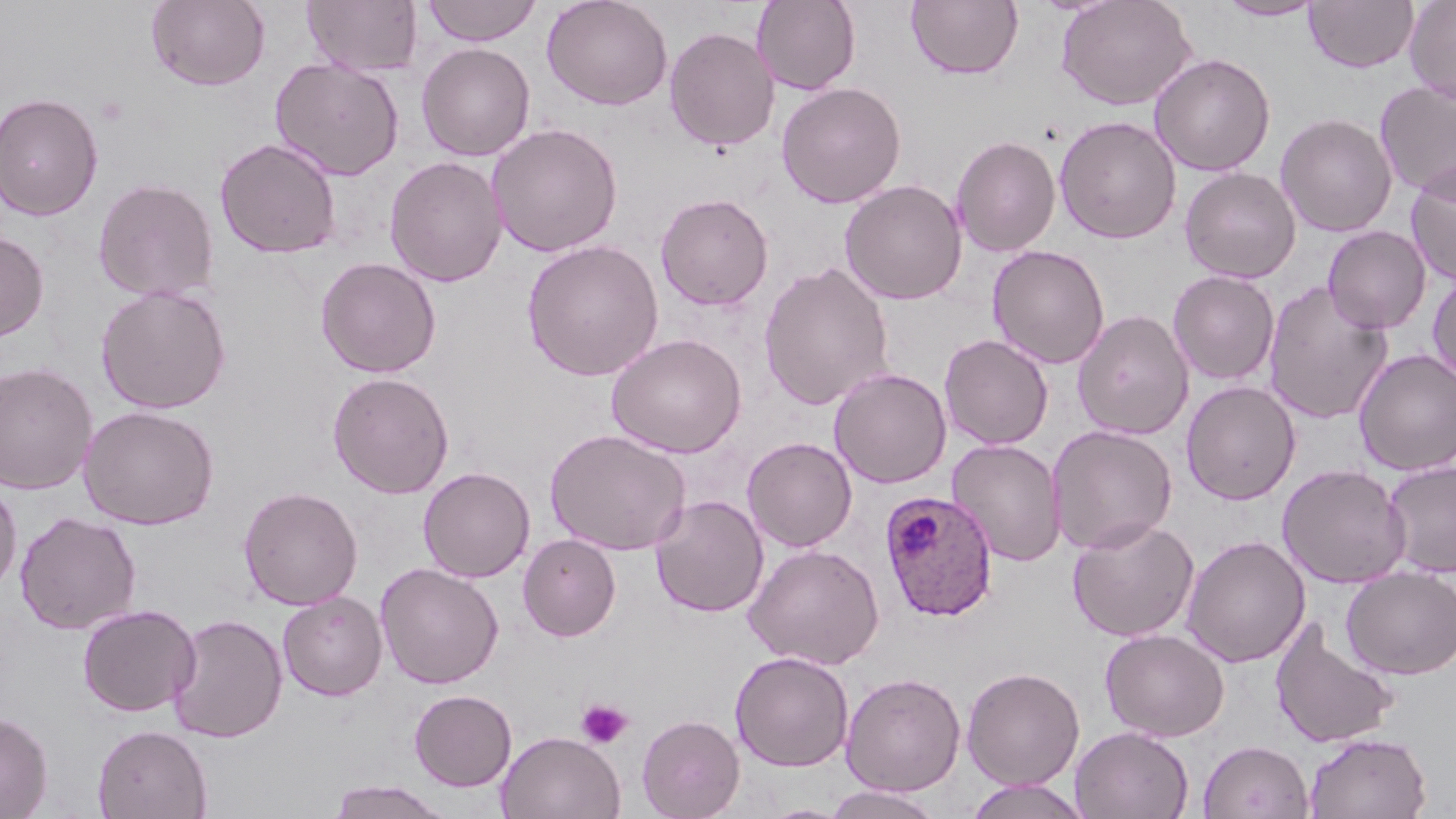
Summary:
  - Coordinate format: approximate bounding boxes as named x1/y1/x2/y2 corners in pixels
  - Plasmodium ovale-infected red blood cell locations: (x1=879, y1=490, x2=999, y2=621)
  - Platelet locations: (x1=576, y1=699, x2=633, y2=748)
  - Uninfected red blood cell locations: (x1=146, y1=0, x2=270, y2=90), (x1=303, y1=0, x2=422, y2=76), (x1=421, y1=0, x2=543, y2=46), (x1=541, y1=0, x2=673, y2=110), (x1=752, y1=0, x2=861, y2=95), (x1=906, y1=0, x2=1023, y2=80), (x1=1055, y1=0, x2=1197, y2=111), (x1=1216, y1=0, x2=1326, y2=20), (x1=1304, y1=0, x2=1419, y2=73), (x1=1403, y1=0, x2=1456, y2=105), (x1=664, y1=26, x2=779, y2=151), (x1=416, y1=42, x2=535, y2=161), (x1=1149, y1=53, x2=1276, y2=176), (x1=269, y1=57, x2=405, y2=181), (x1=776, y1=81, x2=906, y2=208), (x1=1375, y1=81, x2=1456, y2=198), (x1=0, y1=91, x2=104, y2=220), (x1=1275, y1=112, x2=1398, y2=237), (x1=1054, y1=115, x2=1182, y2=244), (x1=487, y1=123, x2=623, y2=257), (x1=950, y1=135, x2=1061, y2=257), (x1=214, y1=137, x2=343, y2=259), (x1=385, y1=156, x2=507, y2=288), (x1=1405, y1=163, x2=1456, y2=286), (x1=1179, y1=166, x2=1301, y2=283), (x1=93, y1=178, x2=219, y2=302), (x1=840, y1=179, x2=967, y2=305), (x1=655, y1=193, x2=773, y2=311), (x1=1323, y1=225, x2=1432, y2=333), (x1=0, y1=230, x2=49, y2=343), (x1=522, y1=239, x2=664, y2=382), (x1=988, y1=245, x2=1110, y2=369), (x1=315, y1=256, x2=442, y2=379), (x1=758, y1=260, x2=895, y2=411), (x1=1168, y1=270, x2=1280, y2=386), (x1=1427, y1=271, x2=1456, y2=385), (x1=1262, y1=281, x2=1395, y2=425), (x1=95, y1=284, x2=232, y2=415), (x1=1072, y1=309, x2=1195, y2=441), (x1=606, y1=332, x2=747, y2=458), (x1=939, y1=334, x2=1054, y2=450), (x1=1353, y1=348, x2=1456, y2=476), (x1=0, y1=362, x2=98, y2=494), (x1=829, y1=367, x2=951, y2=488), (x1=327, y1=371, x2=455, y2=499), (x1=1180, y1=380, x2=1301, y2=505), (x1=79, y1=405, x2=219, y2=530), (x1=1046, y1=424, x2=1178, y2=555), (x1=544, y1=428, x2=691, y2=556), (x1=742, y1=436, x2=858, y2=552), (x1=946, y1=439, x2=1067, y2=566), (x1=1381, y1=459, x2=1456, y2=578), (x1=1277, y1=463, x2=1412, y2=589), (x1=417, y1=466, x2=535, y2=583), (x1=0, y1=479, x2=22, y2=598), (x1=238, y1=485, x2=363, y2=610), (x1=650, y1=495, x2=769, y2=617), (x1=14, y1=511, x2=141, y2=634), (x1=1067, y1=516, x2=1200, y2=642), (x1=518, y1=534, x2=621, y2=641), (x1=1181, y1=535, x2=1311, y2=668), (x1=743, y1=543, x2=885, y2=670), (x1=376, y1=562, x2=504, y2=689), (x1=1341, y1=566, x2=1456, y2=679), (x1=278, y1=591, x2=388, y2=701), (x1=77, y1=603, x2=201, y2=717), (x1=167, y1=613, x2=288, y2=743), (x1=1269, y1=619, x2=1401, y2=748), (x1=1100, y1=628, x2=1230, y2=742), (x1=730, y1=651, x2=854, y2=772), (x1=961, y1=666, x2=1085, y2=790), (x1=840, y1=672, x2=966, y2=797), (x1=408, y1=689, x2=517, y2=791), (x1=0, y1=712, x2=53, y2=818), (x1=636, y1=714, x2=745, y2=819), (x1=93, y1=724, x2=212, y2=819), (x1=1071, y1=726, x2=1194, y2=819), (x1=496, y1=730, x2=626, y2=819), (x1=1304, y1=733, x2=1432, y2=819), (x1=1199, y1=740, x2=1314, y2=819), (x1=964, y1=778, x2=1091, y2=819), (x1=326, y1=779, x2=456, y2=818), (x1=823, y1=785, x2=945, y2=819)
  - Slide-level diagnosis: Plasmodium ovale
  - Modality: optical microscopy
  - Image size: 1456×819 pixels
  - Field of view: single
  - Stain: May-Grünwald-Giemsa
  - Preparation: thin blood film
  - Magnification: 1000x